Name the cell type shown.
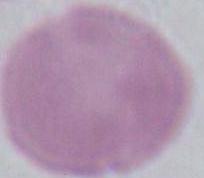
This is an erythrocyte.

{
  "magnification": "1000x",
  "modality": "micrograph"
}